State which parasite is depicted.
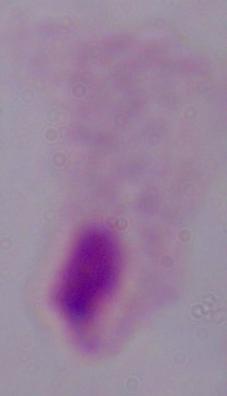
A trichomonad.

Captured at 1000x magnification. Photomicrograph.